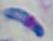
Micrograph. Toxoplasma gondii is seen. 1000x magnification.